Give the extent of all white blood cells.
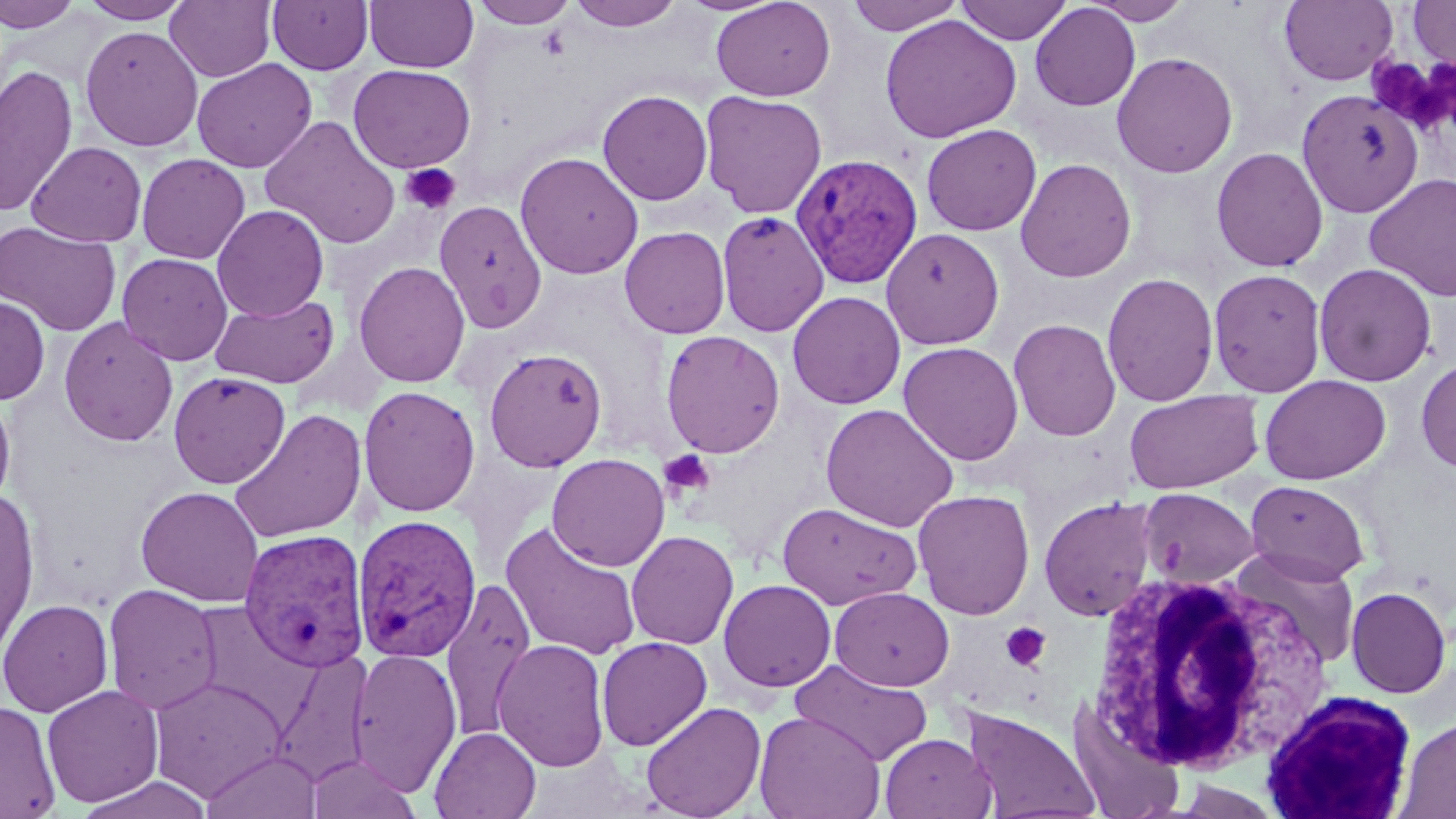

Approximate bounding boxes as [x1, y1, x2, y2] in pixels.
White blood cells: [1087, 570, 1331, 776], [1260, 690, 1419, 819].

Plasmodium vivax-infected red blood cell locations: [790, 153, 924, 288], [353, 514, 482, 663], [237, 528, 370, 674]. Platelet locations: [1370, 56, 1449, 131], [399, 164, 461, 215], [658, 449, 716, 500], [1001, 622, 1052, 672]. Uninfected red blood cell locations: [0, 0, 81, 33], [79, 0, 191, 24], [267, 0, 373, 74], [365, 0, 479, 73], [470, 0, 580, 28], [567, 0, 686, 31], [710, 0, 836, 102], [845, 0, 967, 35], [956, 0, 1073, 45], [1082, 0, 1194, 25], [165, 1, 276, 82], [1278, 1, 1399, 85], [1407, 1, 1456, 75], [1030, 3, 1141, 111], [879, 14, 1021, 143], [80, 25, 203, 152], [1112, 52, 1238, 178], [192, 58, 317, 173], [0, 64, 78, 218], [348, 64, 475, 173], [597, 89, 713, 206], [1295, 89, 1423, 217], [699, 90, 828, 219], [260, 116, 401, 249], [921, 123, 1041, 236], [26, 141, 148, 247], [1210, 147, 1329, 272], [514, 151, 644, 279], [136, 153, 251, 264], [1015, 158, 1137, 282], [1363, 173, 1456, 301], [434, 200, 548, 334], [212, 204, 329, 321], [716, 210, 830, 337], [0, 222, 122, 336], [619, 226, 731, 338], [881, 227, 1005, 349], [117, 252, 233, 365], [354, 261, 470, 388], [1314, 263, 1437, 387], [1208, 268, 1326, 395], [1101, 272, 1219, 406], [787, 291, 905, 409], [210, 294, 339, 388], [0, 295, 51, 405], [58, 317, 179, 447], [1008, 318, 1121, 441], [660, 329, 785, 458], [898, 342, 1024, 466], [483, 347, 607, 471], [1416, 357, 1456, 474], [167, 371, 291, 489], [1259, 375, 1391, 485], [358, 385, 480, 517], [0, 387, 16, 513], [1124, 391, 1263, 494], [820, 403, 960, 532], [228, 408, 366, 545], [546, 453, 670, 571], [1245, 480, 1370, 584], [135, 485, 264, 607], [0, 487, 41, 661], [1138, 487, 1260, 587], [912, 490, 1035, 620], [1038, 496, 1159, 621], [777, 502, 923, 610], [500, 521, 643, 661], [625, 530, 739, 650], [1231, 548, 1362, 671], [440, 577, 537, 743], [718, 579, 837, 692], [103, 583, 223, 715], [829, 586, 954, 692], [1346, 586, 1452, 698], [0, 598, 113, 717], [596, 636, 712, 751], [493, 637, 610, 772], [348, 647, 462, 794], [266, 651, 374, 786], [791, 659, 933, 766], [148, 675, 288, 803], [42, 684, 164, 807], [0, 699, 60, 819], [1065, 699, 1186, 818], [640, 701, 766, 819], [962, 706, 1102, 819], [754, 709, 886, 819], [1397, 716, 1456, 818], [429, 726, 541, 819], [880, 733, 996, 818], [201, 750, 322, 819], [304, 753, 422, 819]. Slide-level diagnosis: Plasmodium vivax. Captured at 1000x magnification. May-Grünwald-Giemsa-stained preparation. Image is 1456×819 pixels. Thin blood smear. Light microscopy. One field of a larger specimen.